Comment on the morphology of the erythrocytes.
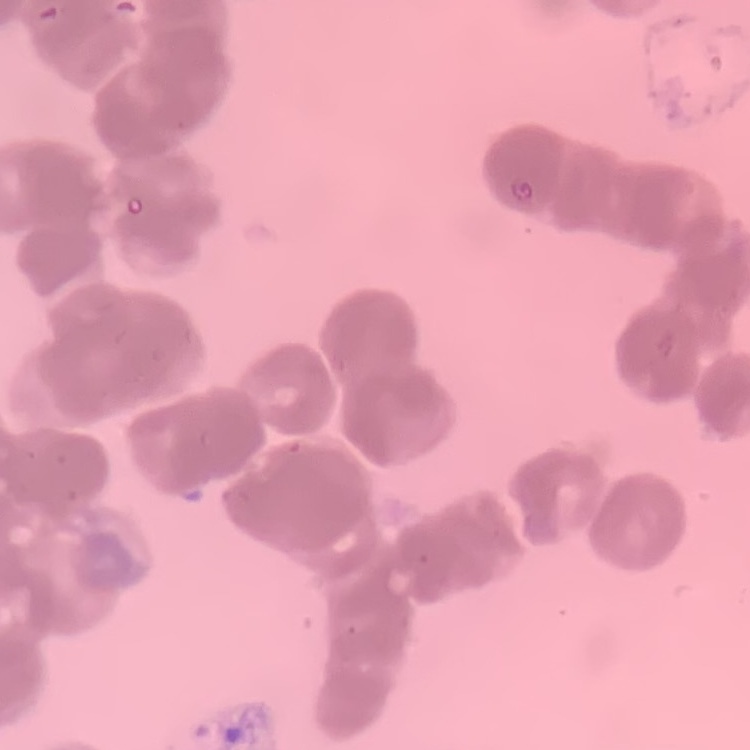
They show rouleaux formation.

stain = Field's or Giemsa
preparation = thin peripheral smear
image type = one tile cut from a larger photomicrograph